Name the blood parasite species.
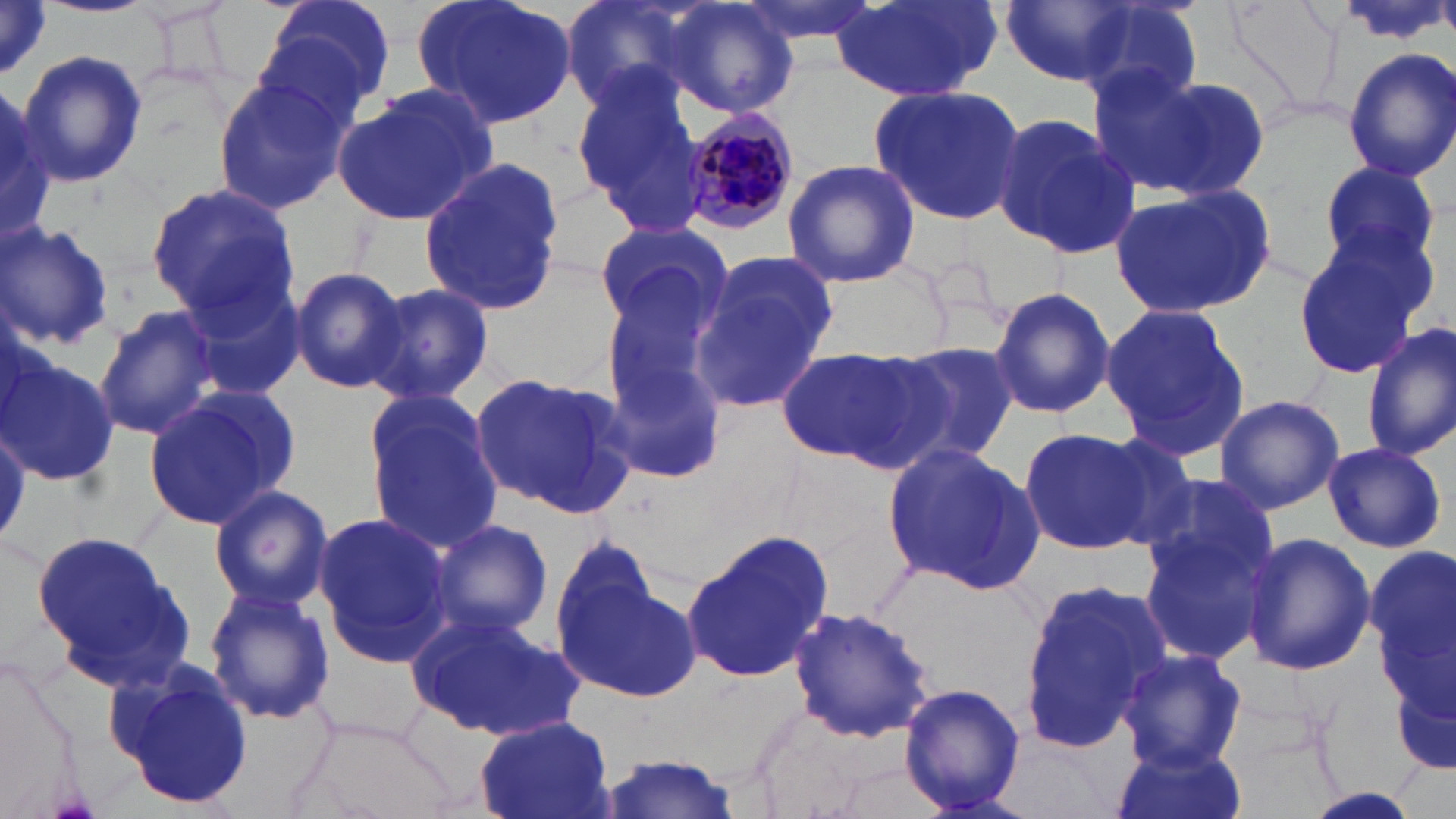
Plasmodium malariae.

Approximate bounding boxes as (x1, y1, x2, y2) in pixels. Uninfected red blood cell locations: (0, 0, 50, 82), (258, 0, 397, 115), (410, 0, 580, 131), (563, 0, 704, 113), (735, 0, 884, 46), (827, 0, 1002, 102), (1000, 0, 1153, 88), (1069, 0, 1204, 111), (658, 2, 799, 119), (16, 49, 146, 187), (1343, 49, 1456, 182), (573, 69, 713, 235), (1108, 70, 1269, 200), (211, 77, 350, 213), (332, 83, 498, 226), (867, 84, 1031, 224), (0, 88, 52, 243), (989, 113, 1139, 258), (781, 159, 920, 287), (1316, 160, 1444, 274), (419, 161, 565, 318), (1111, 180, 1277, 319), (145, 183, 299, 319), (0, 219, 115, 352), (591, 220, 733, 333), (1292, 231, 1432, 381), (689, 251, 840, 415), (288, 267, 407, 393), (599, 277, 724, 421), (180, 279, 305, 404), (361, 281, 494, 408), (988, 284, 1115, 420), (1100, 301, 1253, 462), (94, 307, 223, 438), (1362, 320, 1456, 462), (893, 341, 1019, 465), (774, 345, 938, 467), (601, 352, 729, 487), (2, 354, 119, 489), (468, 372, 638, 517), (142, 384, 302, 528), (360, 386, 502, 548), (1213, 394, 1346, 515), (1018, 426, 1152, 556), (1074, 435, 1203, 551), (883, 441, 1041, 592), (1322, 441, 1447, 554), (1134, 472, 1280, 595), (208, 485, 335, 609), (311, 512, 452, 662), (430, 517, 553, 642), (1136, 523, 1269, 667), (32, 529, 195, 689), (680, 529, 834, 684), (1240, 531, 1375, 676), (551, 532, 662, 651), (1369, 549, 1456, 731), (555, 569, 699, 700), (1017, 577, 1173, 756), (203, 586, 336, 725), (785, 606, 938, 743), (405, 610, 584, 742), (1117, 649, 1246, 772), (106, 657, 257, 811), (897, 681, 1028, 814), (472, 715, 615, 819), (1113, 743, 1244, 819), (590, 755, 747, 817), (1295, 787, 1432, 819). Plasmodium malariae-infected red blood cell locations: (677, 107, 805, 236). May-Grünwald-Giemsa-stained preparation. Image is 1456×819 pixels. Light microscopy. One field of a larger specimen. Captured at 1000x magnification. Thin blood smear.